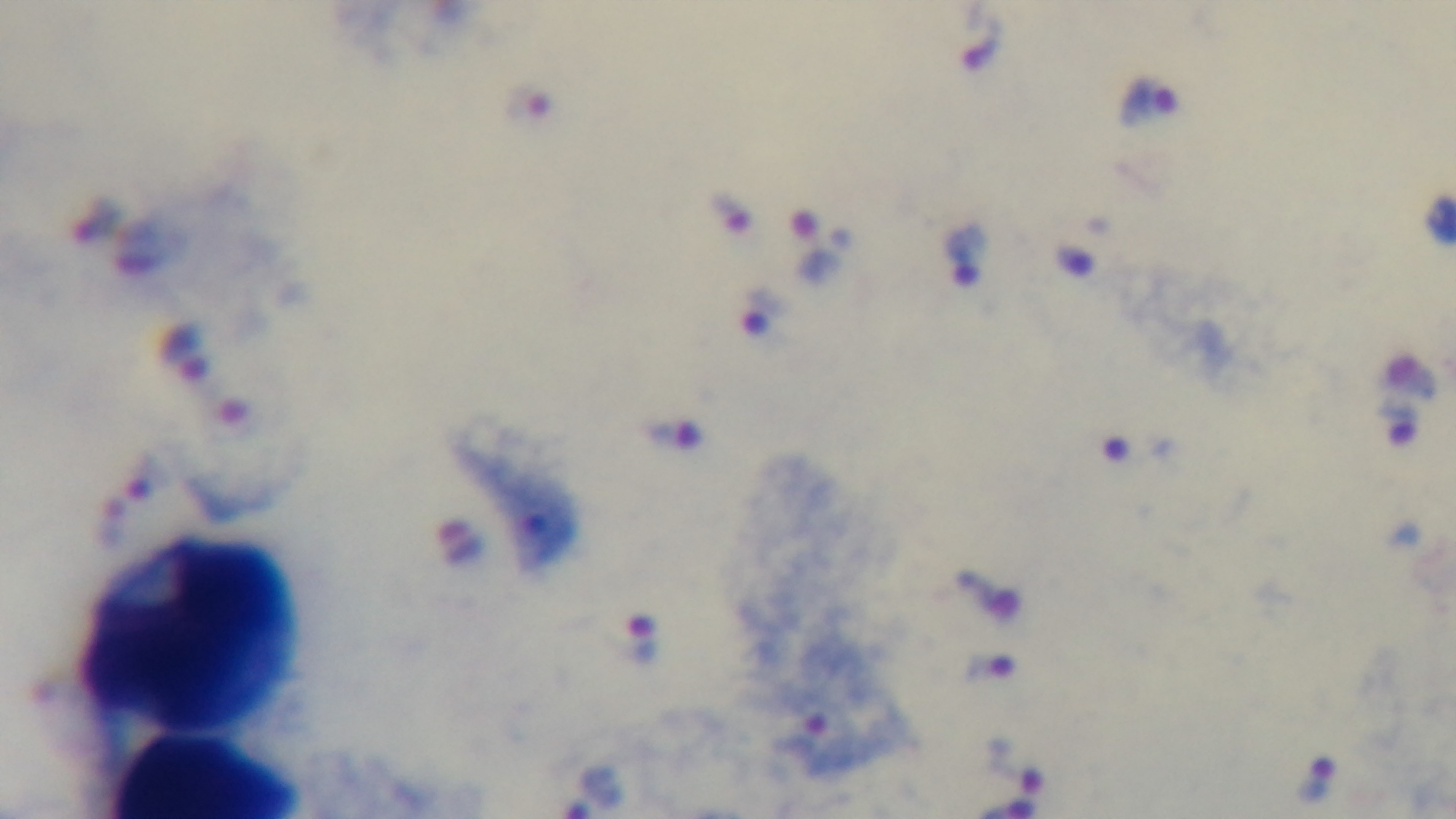

modality = light microscopy
malaria status = positive
field of view = single
stain = Giemsa
objective = 100x oil immersion
preparation = thick blood film
capture = mounted 4K digital camera